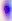
Summary:
  - Modality: micrograph
  - Magnification: 400x
  - Identification: Toxoplasma gondii